Name the parasite shown.
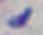
This is Toxoplasma gondii.

Summary:
  - Magnification: 1000x
  - Modality: photomicrograph